Classify this cell by malaria status.
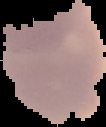

It is uninfected.

preparation = thin blood smear
image type = segmented cell region with the area outside set to black
image size = 106×127 pixels